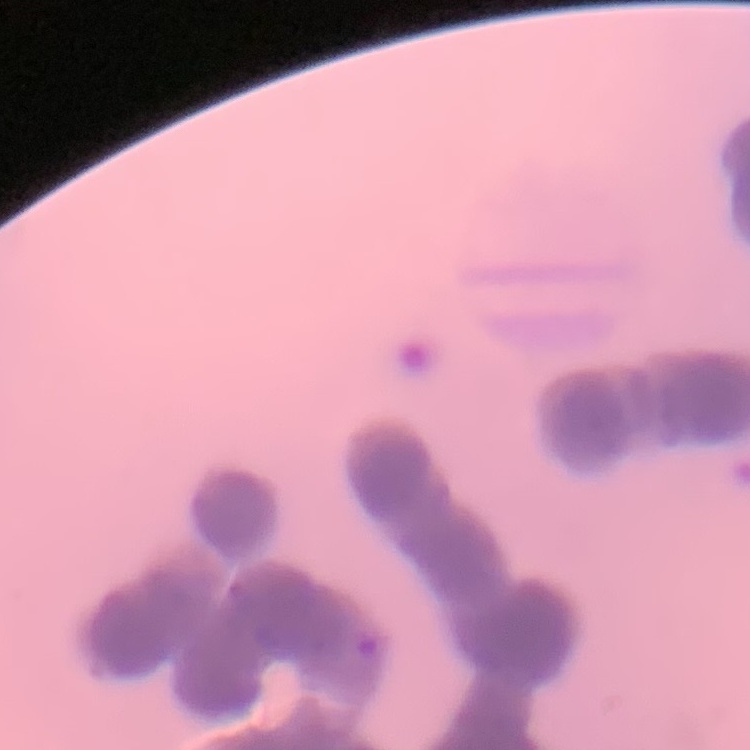
erythrocyte_morphology: rouleaux formation
preparation: thin blood film
stain: Field's or Giemsa
image_type: one tile cut from a larger photomicrograph